Locate every Plasmodium parasite.
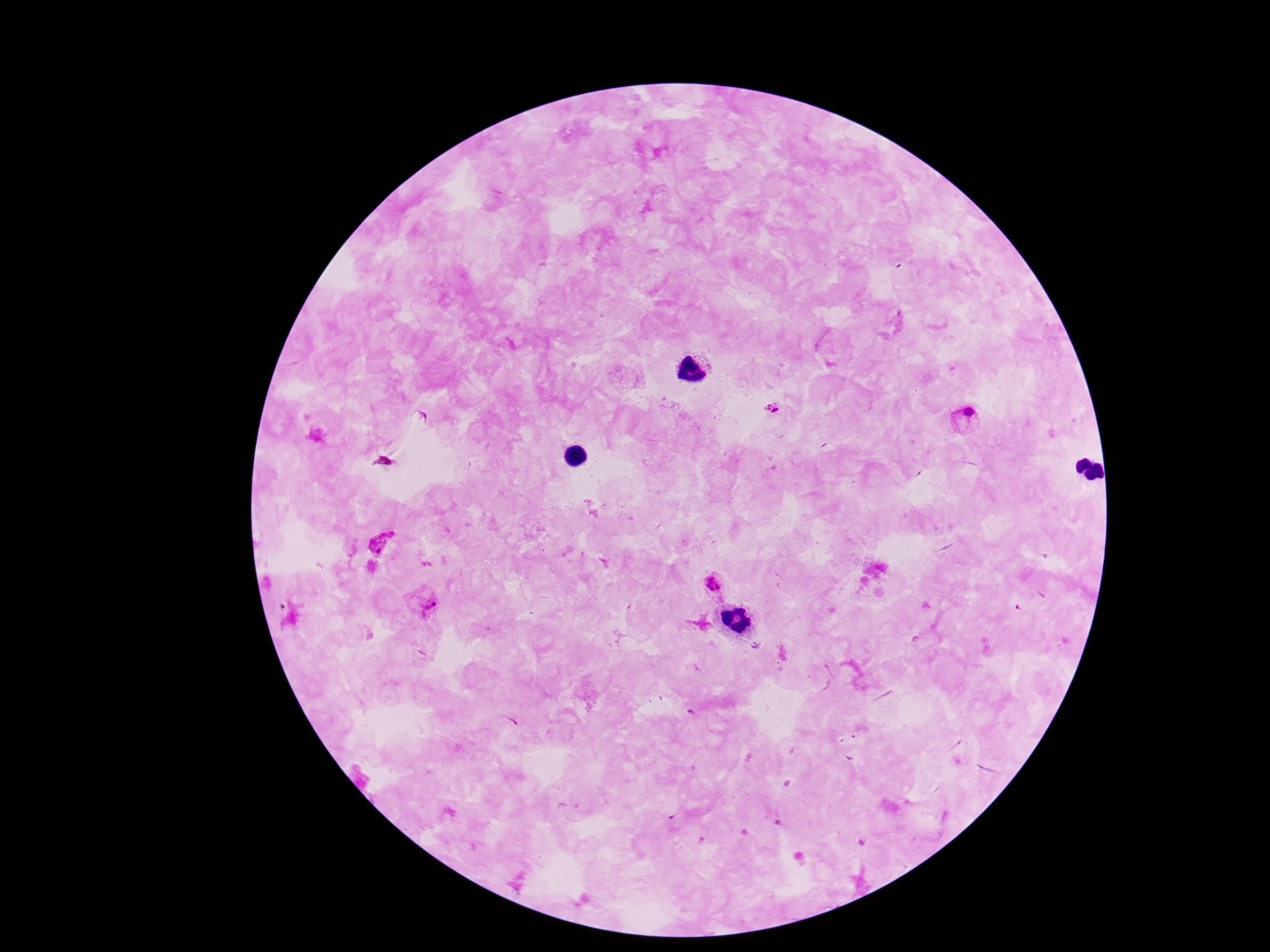

Approximate centers as [x, y] in pixels.
Plasmodium parasites: [772, 408], [968, 420], [380, 543], [715, 586], [424, 601].

{
  "image_size": "1270×952 pixels",
  "patient_malaria_status": "positive",
  "magnification": "100x",
  "stain": "Giemsa",
  "preparation": "thick blood smear",
  "capture": "smartphone camera through the microscope eyepiece",
  "field_of_view": "one from this slide"
}